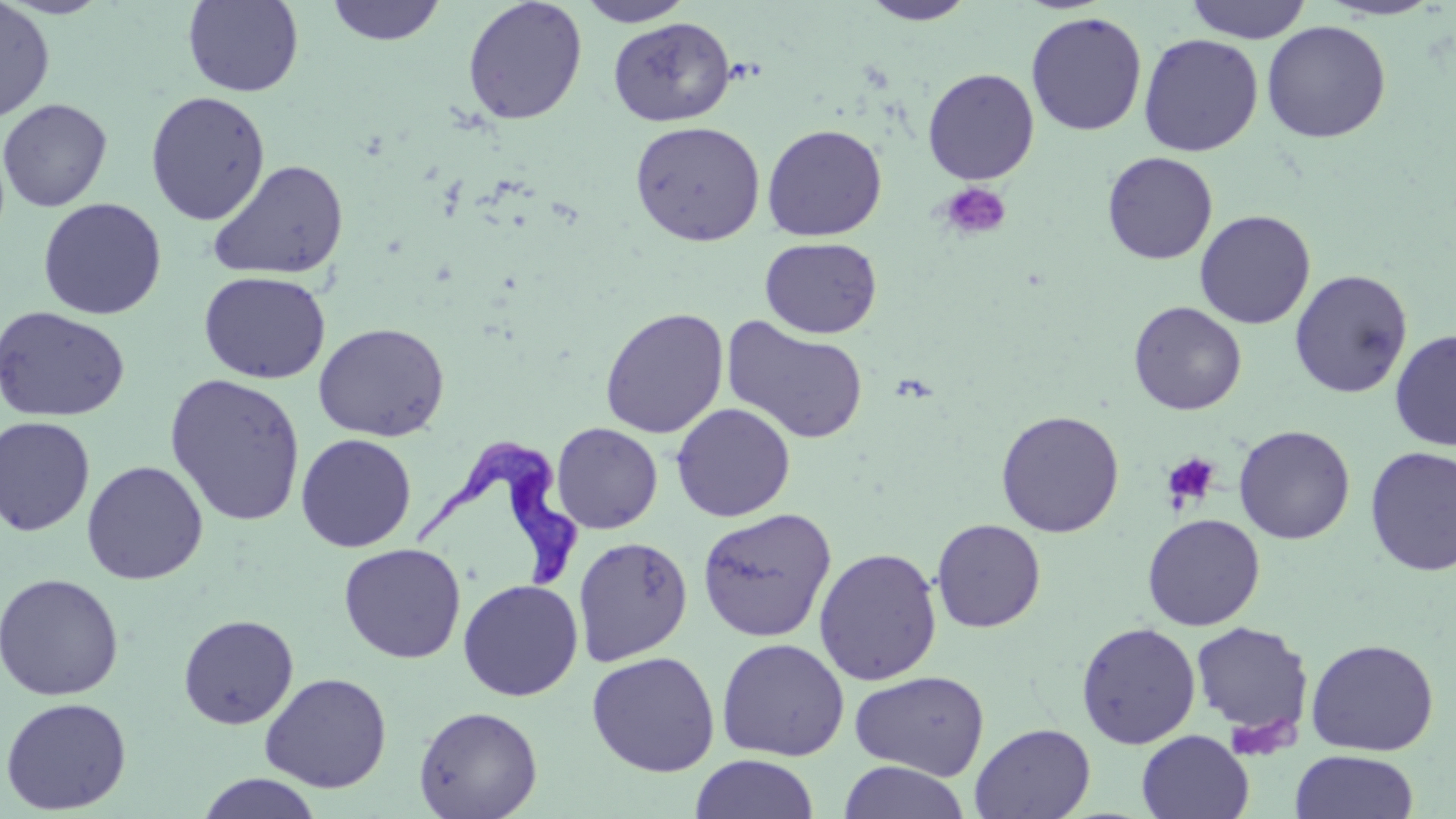

slide_level_diagnosis: Trypanosoma brucei
platelet_locations: 'approximate bounding boxes as named x1/y1/x2/y2 corners in pixels: (x1=939, y1=182, x2=1011, y2=241), (x1=1162, y1=453, x2=1221, y2=511), (x1=1223, y1=713, x2=1298, y2=760)'
trypanosoma_brucei_locations: 'approximate bounding boxes as named x1/y1/x2/y2 corners in pixels: (x1=408, y1=436, x2=582, y2=595)'
field_of_view: single
stain: May-Grünwald-Giemsa
image_size: 1456×819 pixels
modality: optical microscopy
preparation: thin blood smear
uninfected_red_blood_cell_locations: 'approximate bounding boxes as named x1/y1/x2/y2 corners in pixels: (x1=182, y1=0, x2=305, y2=97), (x1=326, y1=0, x2=447, y2=46), (x1=576, y1=0, x2=696, y2=27), (x1=1185, y1=0, x2=1312, y2=43), (x1=0, y1=1, x2=55, y2=122), (x1=462, y1=1, x2=587, y2=124), (x1=859, y1=1, x2=977, y2=25), (x1=1315, y1=1, x2=1447, y2=21), (x1=1025, y1=11, x2=1148, y2=136), (x1=608, y1=17, x2=735, y2=127), (x1=1261, y1=21, x2=1391, y2=143), (x1=1138, y1=33, x2=1263, y2=157), (x1=922, y1=68, x2=1039, y2=185), (x1=145, y1=90, x2=271, y2=225), (x1=0, y1=98, x2=112, y2=213), (x1=629, y1=120, x2=766, y2=246), (x1=762, y1=124, x2=887, y2=241), (x1=1102, y1=152, x2=1218, y2=264), (x1=208, y1=160, x2=349, y2=282), (x1=37, y1=198, x2=167, y2=320), (x1=1194, y1=209, x2=1316, y2=329), (x1=759, y1=236, x2=882, y2=338), (x1=1289, y1=269, x2=1414, y2=398), (x1=198, y1=270, x2=331, y2=384), (x1=1128, y1=301, x2=1246, y2=415), (x1=1, y1=306, x2=130, y2=423), (x1=600, y1=307, x2=729, y2=439), (x1=721, y1=316, x2=870, y2=445), (x1=312, y1=322, x2=450, y2=442), (x1=1389, y1=329, x2=1456, y2=450), (x1=164, y1=373, x2=307, y2=528), (x1=671, y1=402, x2=796, y2=522), (x1=995, y1=409, x2=1125, y2=538), (x1=0, y1=416, x2=96, y2=536), (x1=550, y1=422, x2=663, y2=534), (x1=1234, y1=425, x2=1355, y2=544), (x1=295, y1=433, x2=417, y2=553), (x1=1364, y1=446, x2=1456, y2=576), (x1=81, y1=460, x2=208, y2=585), (x1=697, y1=508, x2=836, y2=642), (x1=1142, y1=513, x2=1265, y2=631), (x1=931, y1=519, x2=1046, y2=633), (x1=573, y1=536, x2=693, y2=666), (x1=339, y1=543, x2=466, y2=663), (x1=813, y1=546, x2=942, y2=686), (x1=0, y1=573, x2=125, y2=702), (x1=458, y1=578, x2=583, y2=701), (x1=178, y1=613, x2=299, y2=729), (x1=1190, y1=621, x2=1313, y2=739), (x1=1076, y1=622, x2=1201, y2=749), (x1=716, y1=637, x2=850, y2=761), (x1=1305, y1=638, x2=1439, y2=756), (x1=586, y1=650, x2=721, y2=777), (x1=850, y1=670, x2=990, y2=781), (x1=259, y1=672, x2=392, y2=793), (x1=0, y1=696, x2=132, y2=815), (x1=413, y1=706, x2=543, y2=818), (x1=970, y1=722, x2=1095, y2=818), (x1=1137, y1=729, x2=1254, y2=819), (x1=1289, y1=750, x2=1419, y2=819), (x1=690, y1=754, x2=819, y2=819), (x1=837, y1=761, x2=971, y2=819), (x1=196, y1=772, x2=323, y2=818)'
magnification: 1000x